Identify the parasite.
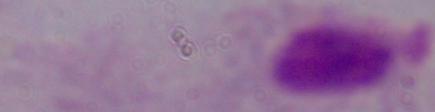

This is a trichomonad.

modality = photomicrograph
magnification = 1000x